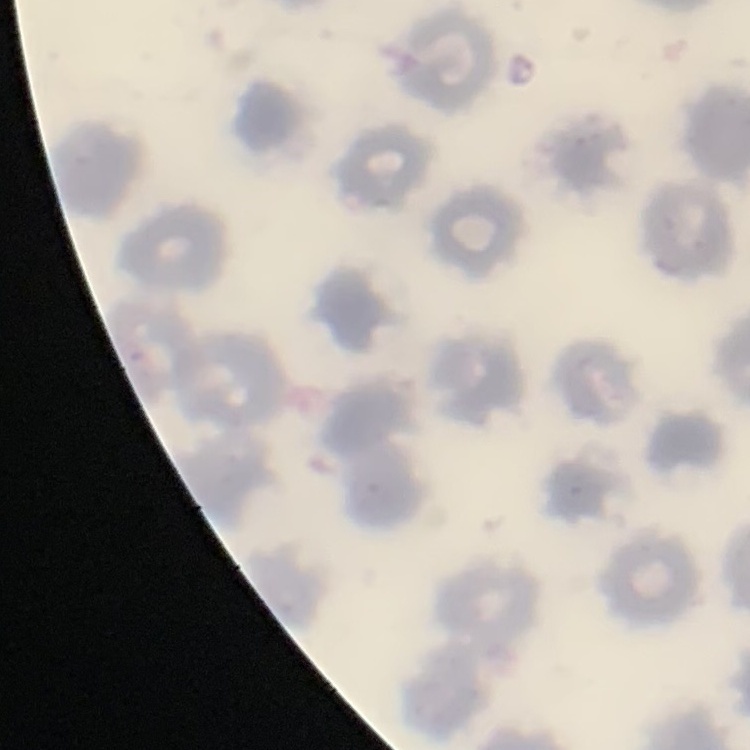
Summary:
  - Erythrocyte morphology: no rouleaux formation
  - Image type: square crop of a larger photomicrograph
  - Preparation: thin blood film
  - Stain: Field's or Giemsa